Assess this cell for malaria.
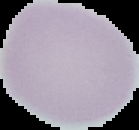

Uninfected.

Summary:
  - Preparation: thin blood film
  - Image type: segmented cell region on a black background
  - Image size: 139×130 pixels